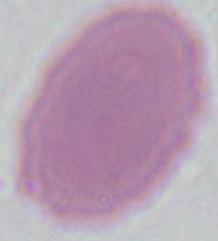

identification = red blood cell
modality = micrograph
magnification = 1000x